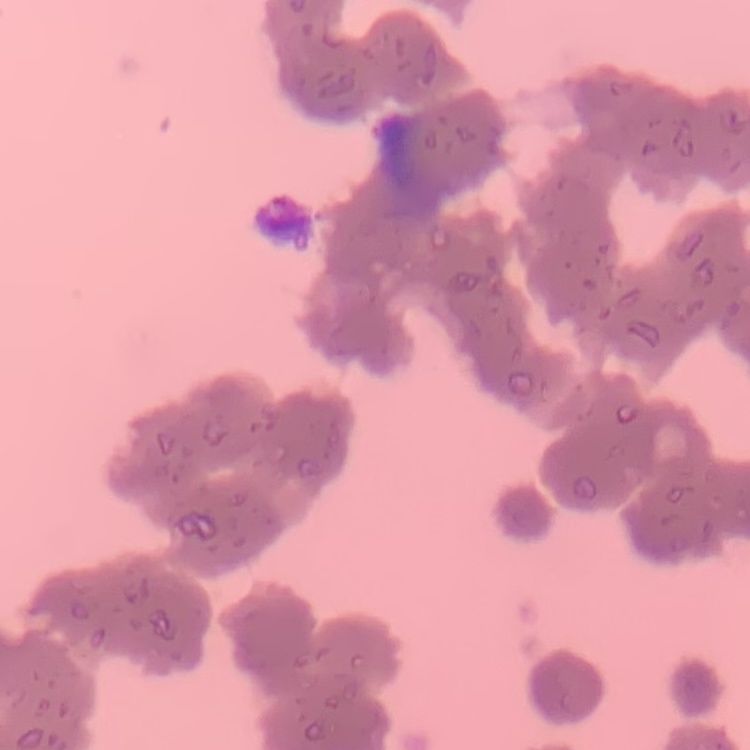
erythrocyte morphology = rouleaux formation
preparation = thin blood film
image type = one tile cut from a larger photomicrograph
stain = Field's or Giemsa